State which parasite is depicted.
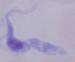
This is a trypanosome.

magnification = 1000x
modality = micrograph